Give the position of every Plasmodium parasite.
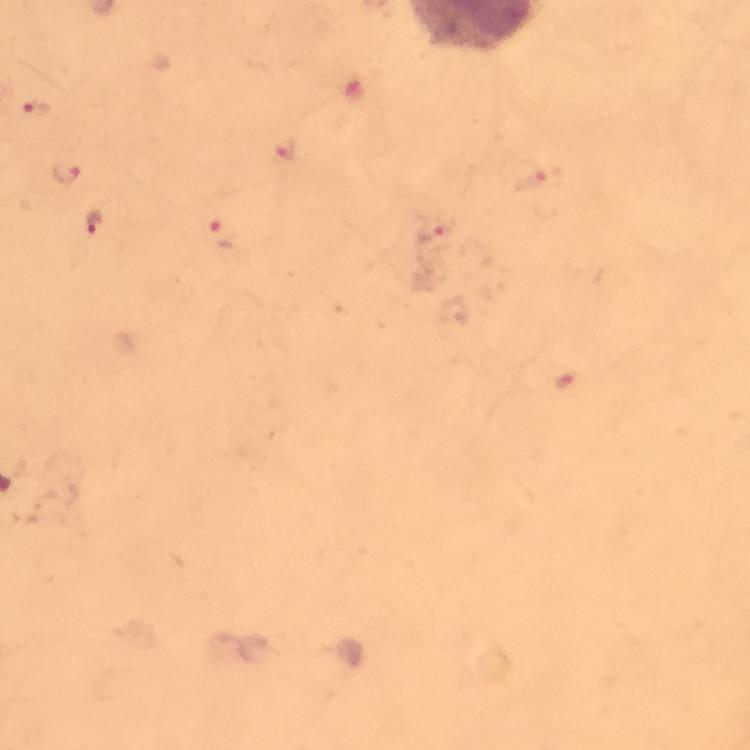

Approximate object centers, in pixels from the top-left corner.
Plasmodium parasites: (x=36, y=111), (x=284, y=151), (x=69, y=175), (x=539, y=180), (x=96, y=223), (x=434, y=231), (x=222, y=234), (x=564, y=381).

Thick smear. Smartphone photograph taken through a microscope. 100x magnification. Image is 750×750 pixels. Immersion oil was used. A crop from one field of view. Giemsa stain. From a malaria diagnostic workup.